Report the malaria status of this cell.
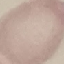
It is uninfected.

Summary:
  - Preparation: thin blood film
  - Capture: smartphone camera at the microscope eyepiece
  - Stain: Giemsa
  - Image type: cell patch, automatically extracted from a larger field of view and resized to 64 × 64 pixels